Report the malaria status of this cell.
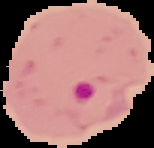
Parasitized.

Summary:
  - Image type: segmented cell region with the area outside set to black
  - Image size: 154×148 pixels
  - Preparation: thin blood smear